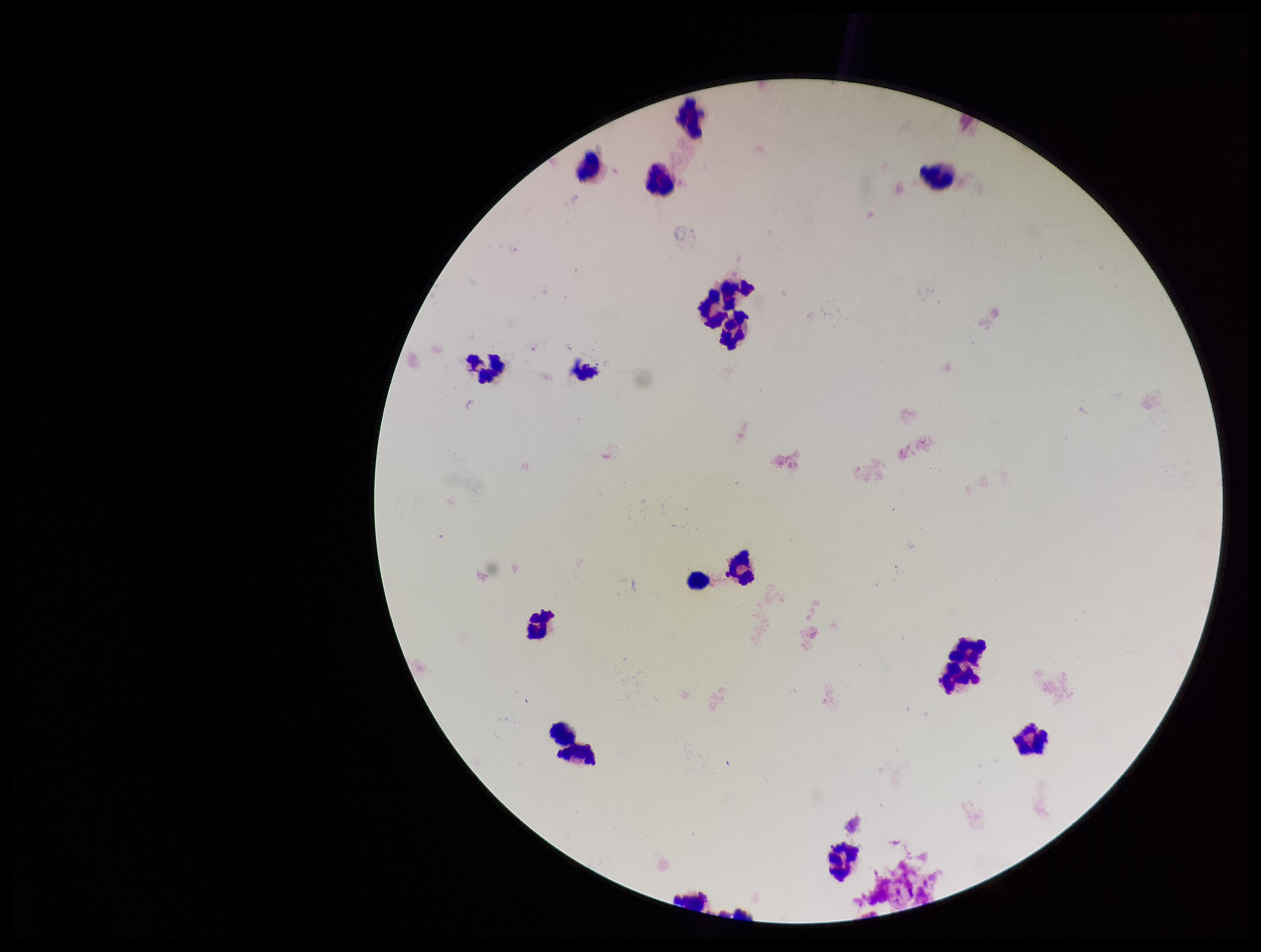
Summary:
  - Image size: 1261×952 pixels
  - Leukocyte count: 16
  - Stain: Giemsa
  - Parasite count: 0
  - Plasmodium parasites: none identified
  - Patient malaria status: negative
  - Field of view: one from this slide
  - Capture: smartphone photograph through the microscope eyepiece
  - Preparation: thick blood smear